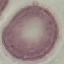

Summary:
  - Result: no malaria parasites detected
  - Image type: cell patch, automatically extracted from a larger field of view and resized to 64 × 64 pixels
  - Preparation: thin smear
  - Capture: smartphone through the microscope eyepiece
  - Stain: Giemsa